State which parasite is depicted.
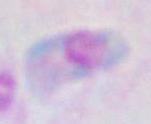
Toxoplasma gondii.

{
  "magnification": "1000x",
  "modality": "photomicrograph"
}